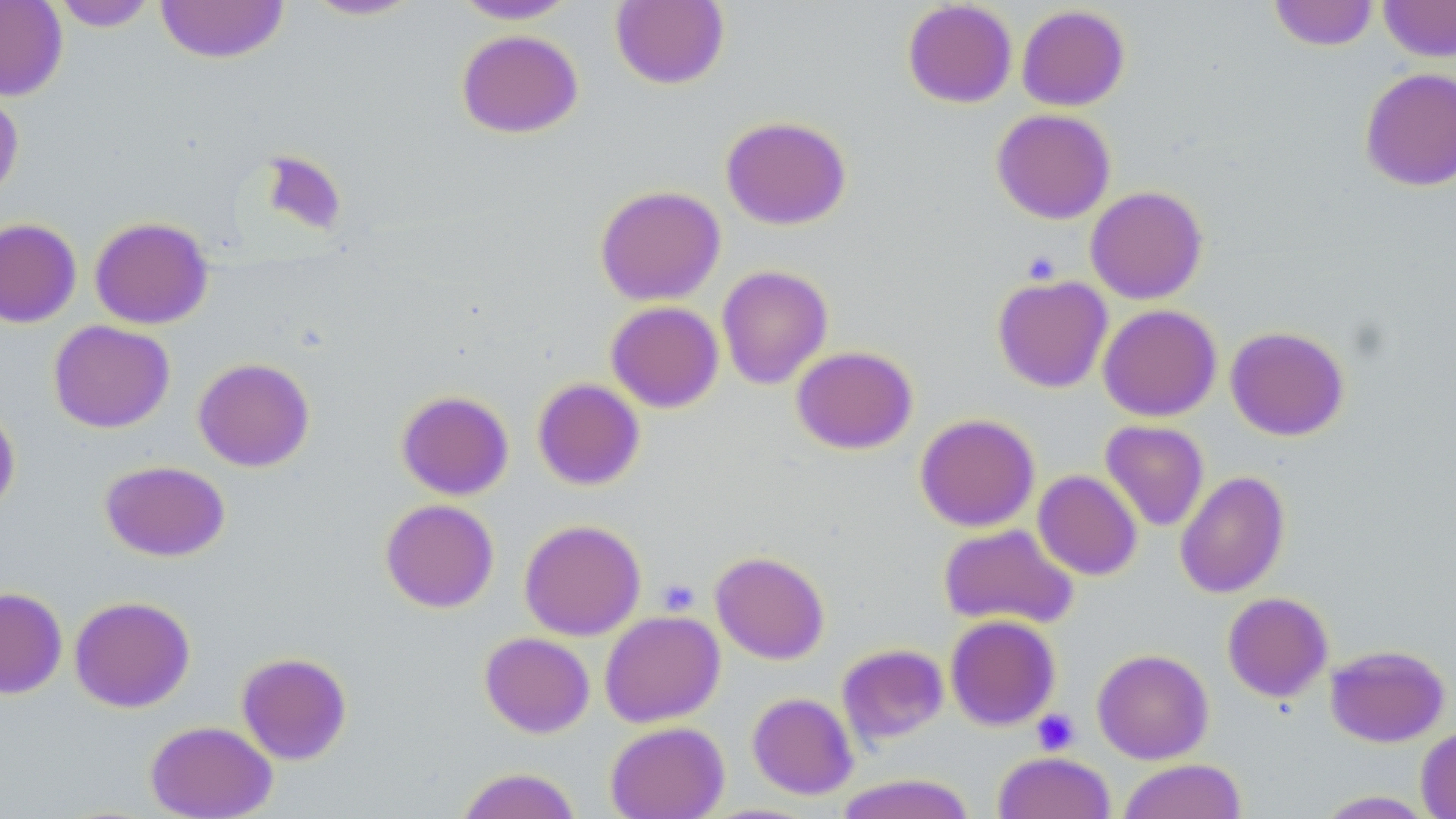

Approximate bounding boxes as [x1, y1, x2, y2] in pixels. Platelet locations: [656, 577, 700, 616], [1031, 709, 1080, 755]. Uninfected red blood cell locations: [0, 0, 68, 101], [450, 0, 581, 24], [610, 0, 730, 90], [1268, 0, 1378, 51], [1378, 0, 1456, 62], [50, 1, 159, 32], [155, 1, 290, 64], [302, 1, 425, 21], [902, 1, 1017, 108], [1016, 5, 1129, 111], [456, 29, 584, 138], [1359, 67, 1456, 192], [0, 85, 24, 203], [991, 108, 1116, 224], [721, 115, 851, 230], [259, 151, 347, 236], [595, 185, 725, 306], [1085, 185, 1208, 304], [89, 216, 213, 329], [0, 218, 82, 328], [717, 265, 833, 390], [992, 275, 1112, 392], [605, 301, 724, 413], [1098, 304, 1221, 421], [48, 320, 175, 433], [1225, 325, 1349, 441], [791, 346, 917, 454], [193, 357, 315, 472], [532, 378, 645, 490], [396, 390, 514, 500], [0, 404, 21, 515], [915, 412, 1039, 532], [1100, 420, 1210, 531], [99, 460, 230, 562], [1033, 470, 1142, 580], [1174, 470, 1290, 598], [380, 498, 499, 613], [519, 519, 646, 641], [938, 523, 1079, 630], [710, 550, 830, 664], [0, 587, 67, 699], [1222, 592, 1333, 702], [69, 595, 195, 713], [599, 610, 724, 727], [945, 614, 1061, 731], [479, 632, 595, 738], [837, 644, 949, 746], [1325, 644, 1450, 747], [1092, 648, 1213, 764], [236, 652, 352, 765], [747, 692, 858, 800], [145, 720, 278, 818], [605, 721, 729, 819], [1416, 726, 1456, 819], [992, 751, 1116, 819], [1117, 759, 1247, 819], [454, 767, 583, 819], [834, 773, 978, 819], [1313, 789, 1438, 818]. Slide-level diagnosis: negative for blood parasites. Single field of view. Captured at 1000x magnification. Optical microscopy. Image is 1456×819 pixels. May-Grünwald-Giemsa stain. Thin blood smear.